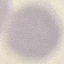
result = no malaria parasites seen
capture = smartphone through the microscope eyepiece
preparation = thin blood film
stain = Giemsa
image type = automatically extracted cell patch, resized to 64 × 64 pixels